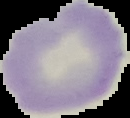 Image is 130×118 pixels. Cell region segmented out of the field of view; the surrounding area is masked to black. Result: negative for Plasmodium parasites. From a thin blood film.